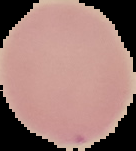

{
  "image_type": "segmented cell region with the area outside set to black",
  "image_size": "136×151 pixels",
  "preparation": "thin blood film",
  "result": "no malaria parasites detected"
}